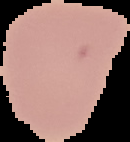
Summary:
  - Image size: 130×142 pixels
  - Malaria status: uninfected
  - Preparation: thin blood smear
  - Image type: cell region segmented out of the field of view; surrounding area masked to black